Comment on the morphology of the erythrocytes.
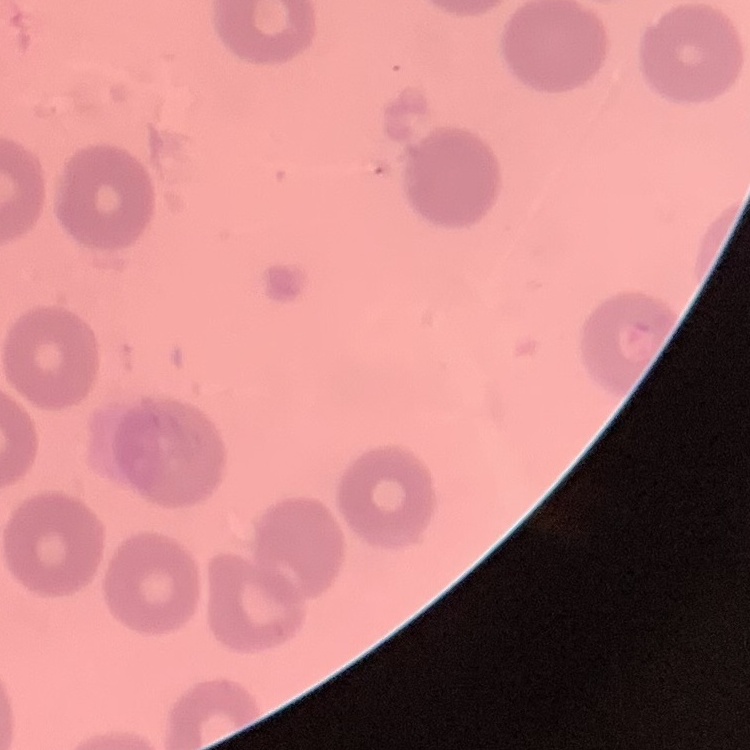
They show no rouleaux formation.

Summary:
  - Preparation: thin peripheral smear
  - Image type: square crop of a larger photomicrograph
  - Stain: Field's or Giemsa